Assess this cell for malaria.
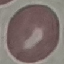

It is uninfected.

{
  "preparation": "thin blood smear",
  "image_type": "automatically extracted cell patch, resized to 64 × 64 pixels",
  "stain": "Giemsa",
  "capture": "smartphone camera at the microscope eyepiece"
}